Classify this cell by malaria status.
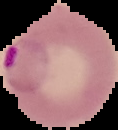
It is parasitized.

Summary:
  - Image size: 118×130 pixels
  - Image type: segmented cell region with the area outside set to black
  - Preparation: thin blood film